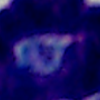 Photomicrograph. Captured at 1000x magnification. A white blood cell is seen.